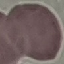

Summary:
  - Result: no malaria parasites detected
  - Capture: smartphone camera at the microscope eyepiece
  - Preparation: thin blood film
  - Image type: cell patch, automatically extracted from a larger field of view and resized to 64 × 64 pixels
  - Stain: Giemsa